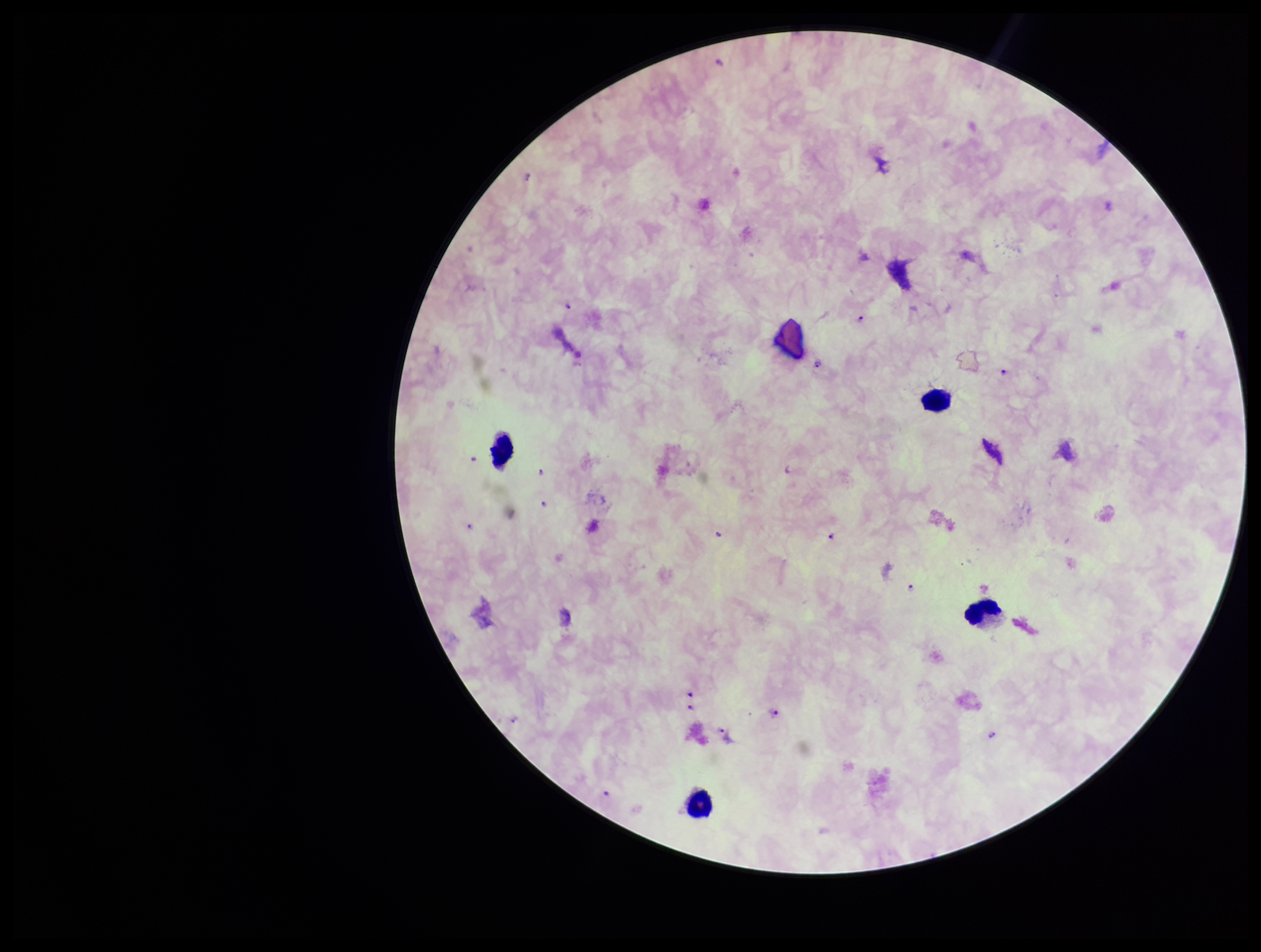

{
  "stain": "Giemsa",
  "capture": "smartphone photograph through the microscope eyepiece",
  "leukocyte_count": 4,
  "field_of_view": "one from this slide",
  "preparation": "thick smear",
  "species_reported_for_this_patient": "Plasmodium falciparum",
  "plasmodium_parasites": "detected",
  "patient_malaria_status": "positive",
  "parasite_count": 17,
  "image_size": "1261×952 pixels"
}